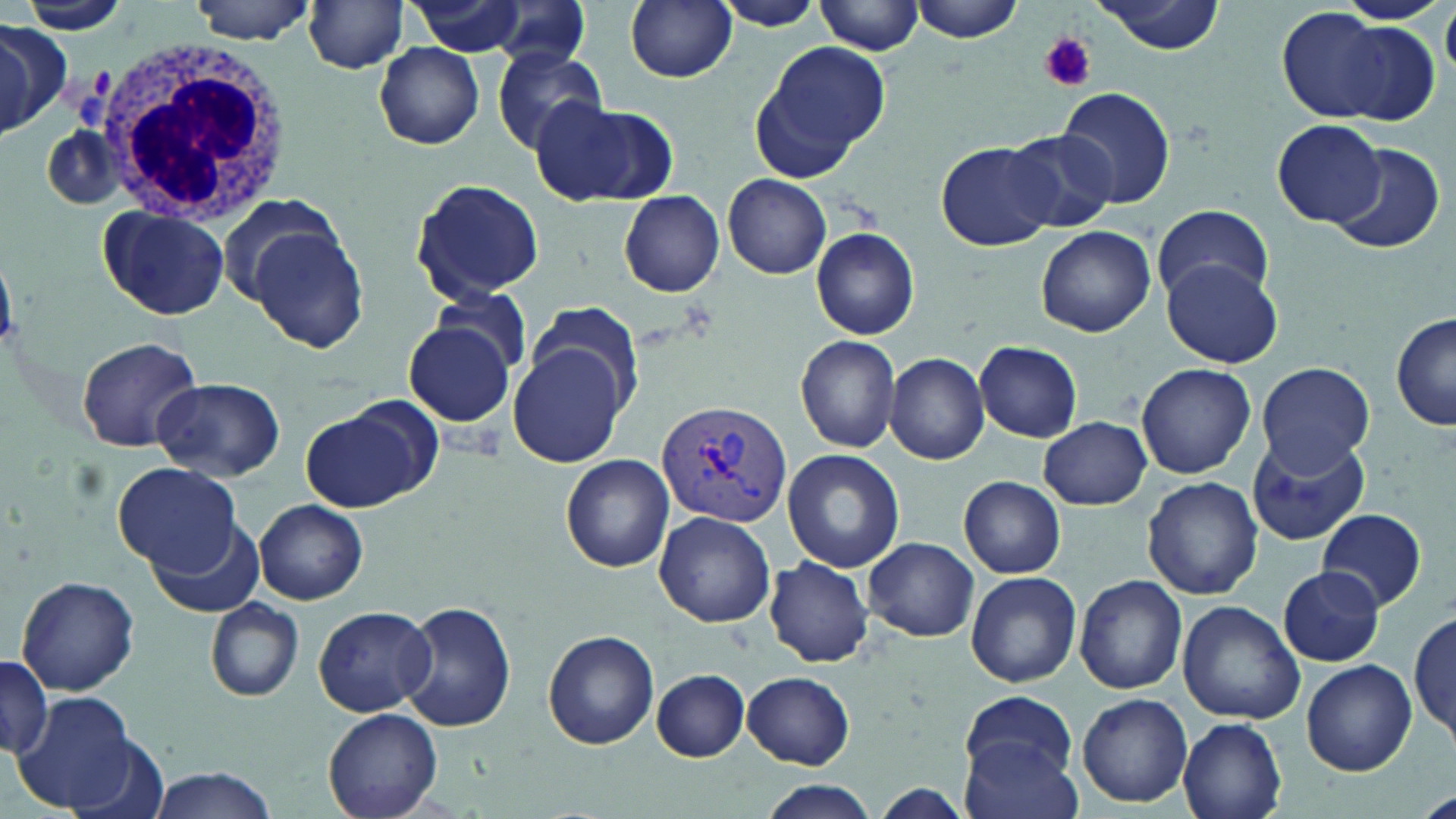
Summary:
  - Coordinate format: approximate bounding boxes as [x1, y1, x2, y2] in pixels
  - Plasmodium vivax-infected red blood cell locations: [655, 399, 793, 530]
  - White blood cell locations: [91, 34, 290, 226]
  - Uninfected red blood cell locations: [186, 0, 322, 43], [407, 0, 536, 56], [715, 0, 830, 31], [818, 0, 925, 56], [906, 0, 1026, 43], [1096, 0, 1228, 55], [1338, 0, 1449, 24], [625, 1, 737, 84], [13, 3, 133, 34], [302, 3, 411, 74], [483, 3, 596, 71], [1282, 11, 1436, 125], [0, 22, 64, 135], [374, 41, 485, 149], [753, 41, 888, 178], [490, 47, 610, 154], [1057, 86, 1177, 210], [531, 98, 673, 206], [1272, 119, 1387, 228], [1004, 127, 1118, 233], [935, 139, 1057, 251], [1330, 143, 1446, 253], [724, 175, 830, 278], [411, 177, 545, 302], [620, 191, 725, 296], [214, 192, 344, 309], [1152, 203, 1272, 305], [97, 206, 231, 319], [247, 224, 370, 354], [1035, 226, 1156, 338], [810, 228, 919, 341], [1163, 257, 1282, 369], [428, 285, 536, 382], [523, 303, 648, 421], [1392, 313, 1456, 432], [404, 321, 517, 429], [75, 335, 204, 451], [795, 335, 902, 453], [509, 340, 632, 469], [975, 341, 1082, 441], [884, 353, 989, 464], [1135, 362, 1257, 479], [1255, 362, 1376, 474], [153, 377, 286, 480], [300, 405, 433, 513], [1038, 416, 1152, 510], [1246, 434, 1372, 547], [782, 449, 905, 574], [559, 454, 675, 572], [113, 462, 239, 574], [958, 476, 1066, 579], [1142, 476, 1264, 601], [255, 500, 368, 604], [1318, 508, 1429, 611], [653, 509, 775, 626], [150, 518, 261, 619], [863, 537, 980, 642], [765, 557, 873, 668], [1278, 567, 1387, 666], [965, 571, 1081, 687], [1073, 574, 1188, 694], [15, 575, 142, 696], [207, 599, 303, 702], [399, 600, 515, 732], [1177, 602, 1305, 724], [312, 606, 436, 716], [1411, 606, 1456, 746], [543, 629, 659, 751], [0, 657, 53, 759], [1299, 660, 1417, 775], [650, 669, 750, 761], [743, 672, 854, 769], [962, 691, 1077, 784], [14, 692, 136, 809], [1075, 693, 1193, 808], [323, 708, 444, 819], [1179, 717, 1287, 819], [67, 735, 174, 819], [961, 736, 1082, 819], [139, 766, 280, 819], [755, 780, 881, 819]
  - Platelet locations: [1038, 32, 1096, 93]
  - Slide-level diagnosis: Plasmodium vivax
  - Stain: May-Grünwald-Giemsa
  - Preparation: thin blood smear
  - Image size: 1456×819 pixels
  - Magnification: 1000x
  - Field of view: one of a larger specimen
  - Modality: optical microscopy